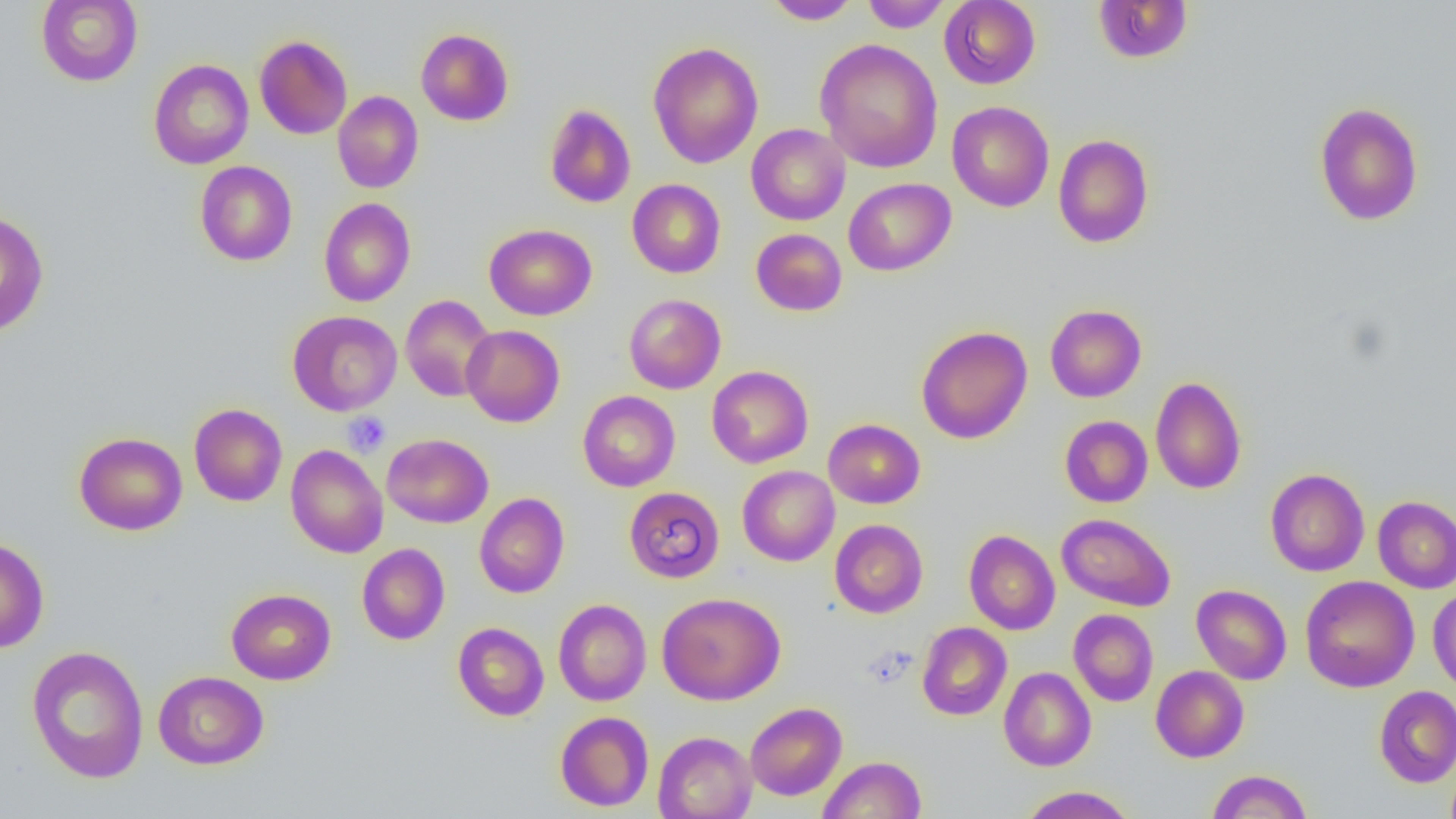

Summary:
  - Coordinate format: approximate bounding boxes as [x1, y1, x2, y2] in pixels
  - Platelet locations: [342, 412, 390, 457], [863, 645, 917, 687]
  - Uninfected red blood cell locations: [35, 0, 143, 86], [861, 0, 951, 32], [938, 0, 1040, 89], [764, 1, 860, 25], [1092, 1, 1195, 64], [416, 28, 514, 126], [254, 35, 353, 139], [814, 38, 943, 173], [647, 41, 763, 168], [148, 58, 254, 170], [332, 90, 423, 193], [946, 101, 1055, 212], [1313, 101, 1424, 226], [544, 103, 636, 208], [746, 123, 850, 225], [1054, 134, 1154, 248], [194, 160, 297, 266], [843, 178, 956, 276], [627, 179, 725, 278], [318, 197, 416, 307], [0, 209, 49, 337], [484, 223, 597, 320], [751, 228, 847, 316], [400, 294, 497, 402], [624, 294, 726, 393], [1045, 304, 1147, 402], [287, 310, 402, 416], [461, 325, 565, 427], [916, 325, 1032, 444], [706, 365, 813, 468], [1150, 376, 1246, 494], [578, 390, 681, 491], [188, 403, 287, 507], [1060, 415, 1153, 507], [823, 419, 925, 509], [74, 432, 187, 536], [382, 433, 493, 528], [286, 445, 388, 558], [737, 465, 839, 566], [1265, 468, 1370, 576], [624, 486, 725, 583], [475, 493, 569, 598], [1372, 496, 1456, 593], [1056, 513, 1175, 611], [829, 519, 928, 618], [963, 530, 1060, 635], [0, 536, 49, 653], [357, 543, 450, 645], [1300, 575, 1419, 693], [1191, 584, 1292, 684], [1428, 587, 1456, 696], [226, 588, 336, 684], [657, 592, 786, 705], [553, 599, 651, 706], [1069, 609, 1158, 706], [452, 622, 549, 721], [917, 622, 1012, 720], [26, 645, 149, 784], [1151, 665, 1249, 763], [999, 667, 1096, 771], [153, 671, 269, 769], [1374, 686, 1456, 787], [745, 702, 847, 800], [554, 711, 654, 811], [653, 730, 757, 819], [818, 755, 926, 819], [1206, 769, 1313, 818], [1017, 786, 1137, 818]
  - Slide-level diagnosis: no evidence of blood parasites
  - Image size: 1456×819 pixels
  - Field of view: single
  - Magnification: 1000x
  - Modality: optical microscopy
  - Preparation: thin blood film